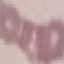
Malaria status: uninfected. Giemsa stain. Thin smear of blood. Automatically extracted cell patch, resized to 64 × 64 pixels. Acquired by smartphone through the microscope eyepiece.